Identify the parasite.
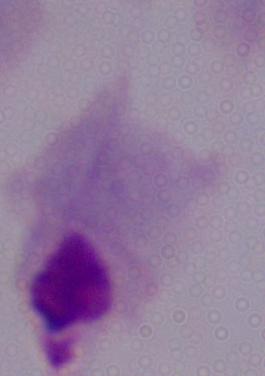
This is a trichomonad.

modality: micrograph
magnification: 1000x